Locate and identify every blood parasite.
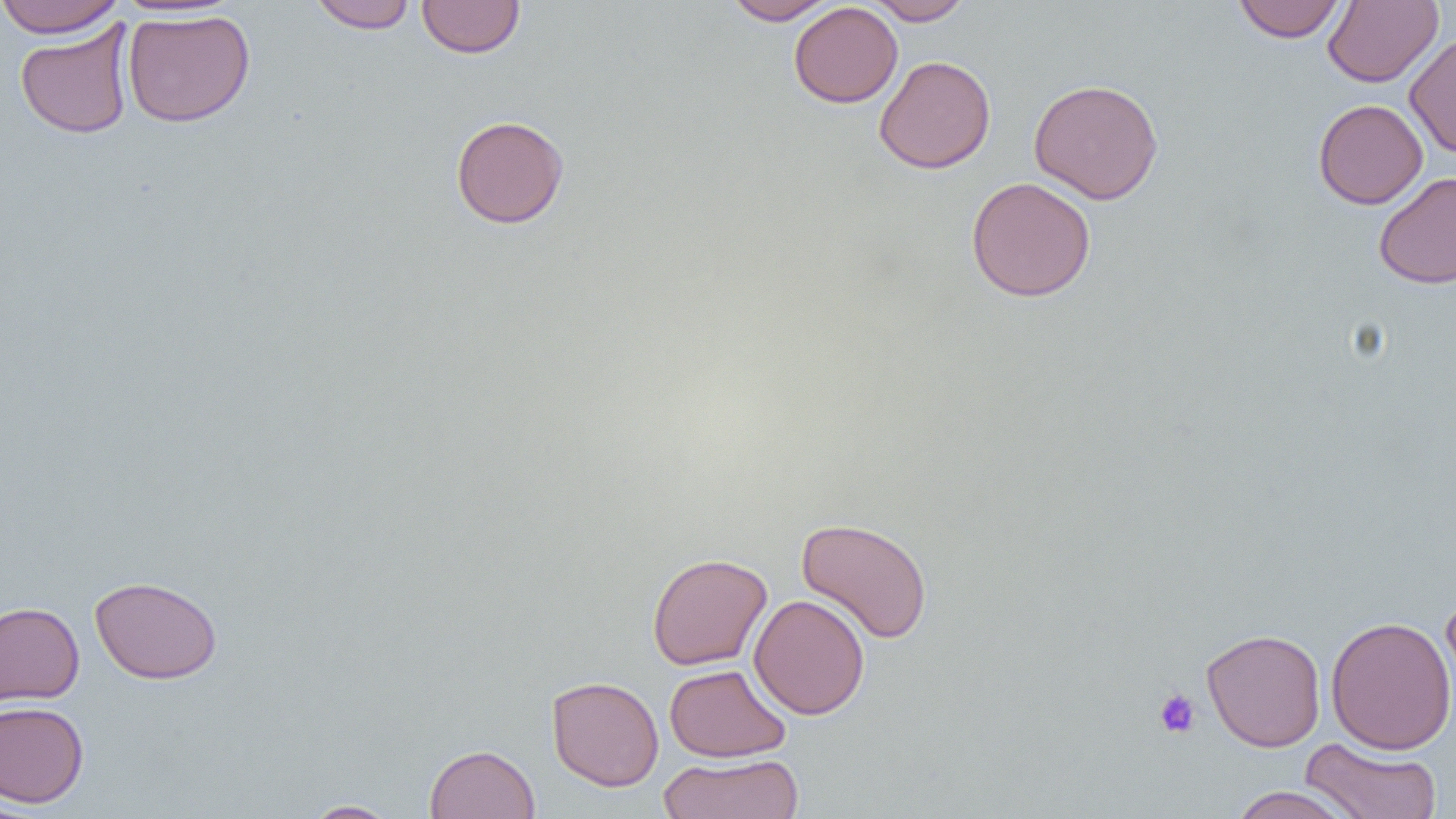

No blood parasites observed.

Approximate bounding boxes as named x1/y1/x2/y2 corners in pixels. Uninfected red blood cell locations: (x1=0, y1=0, x2=125, y2=38), (x1=307, y1=0, x2=419, y2=33), (x1=417, y1=0, x2=525, y2=58), (x1=722, y1=0, x2=838, y2=25), (x1=864, y1=0, x2=972, y2=25), (x1=1233, y1=0, x2=1345, y2=43), (x1=1323, y1=0, x2=1443, y2=87), (x1=789, y1=2, x2=903, y2=108), (x1=122, y1=9, x2=255, y2=128), (x1=15, y1=20, x2=135, y2=139), (x1=1404, y1=34, x2=1456, y2=158), (x1=874, y1=55, x2=996, y2=174), (x1=1029, y1=78, x2=1164, y2=204), (x1=1313, y1=99, x2=1428, y2=209), (x1=450, y1=115, x2=570, y2=229), (x1=1373, y1=172, x2=1456, y2=289), (x1=965, y1=176, x2=1096, y2=302), (x1=796, y1=517, x2=933, y2=644), (x1=647, y1=552, x2=772, y2=670), (x1=89, y1=575, x2=223, y2=684), (x1=1440, y1=589, x2=1456, y2=713), (x1=749, y1=594, x2=870, y2=720), (x1=0, y1=601, x2=84, y2=706), (x1=1325, y1=615, x2=1456, y2=755), (x1=1201, y1=627, x2=1326, y2=752), (x1=664, y1=664, x2=791, y2=762), (x1=546, y1=675, x2=664, y2=791), (x1=0, y1=700, x2=89, y2=808), (x1=1299, y1=737, x2=1443, y2=818), (x1=424, y1=743, x2=541, y2=819), (x1=657, y1=753, x2=805, y2=818), (x1=1227, y1=786, x2=1359, y2=819), (x1=0, y1=794, x2=43, y2=818), (x1=303, y1=800, x2=399, y2=819). Platelet locations: (x1=1153, y1=688, x2=1201, y2=739). Slide-level diagnosis: negative for blood parasites. Light microscopy. Thin blood smear. One field of a larger specimen. 1000x magnification. Image is 1456×819 pixels.